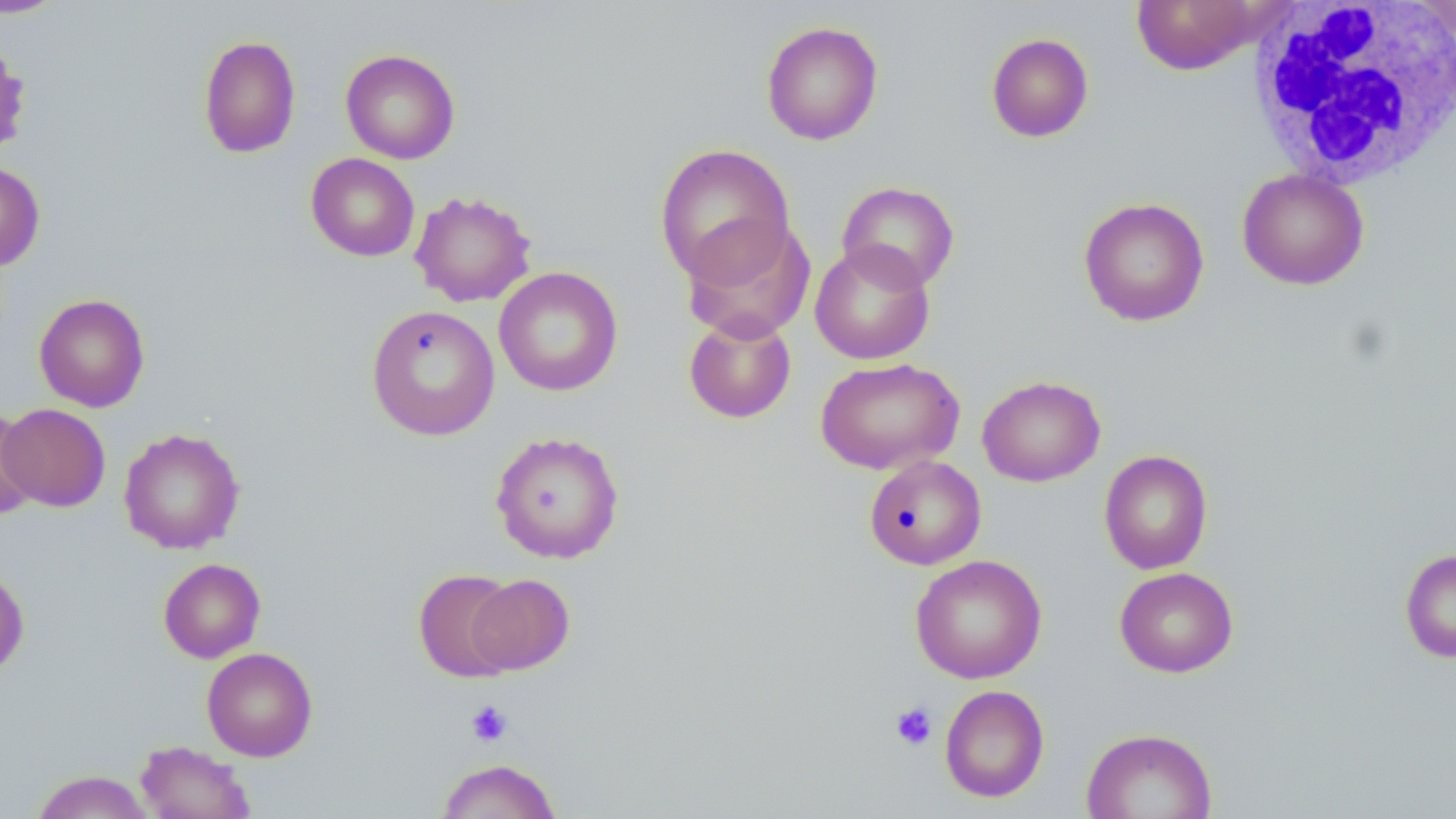

Summary:
  - Coordinate format: approximate bounding boxes as [x1, y1, x2, y2] in pixels
  - Uninfected red blood cell locations: [1128, 0, 1277, 74], [0, 1, 68, 18], [1413, 1, 1456, 43], [761, 21, 883, 145], [986, 32, 1094, 142], [197, 34, 301, 158], [340, 48, 460, 164], [654, 143, 796, 285], [305, 153, 419, 261], [0, 161, 45, 272], [1237, 168, 1369, 290], [836, 181, 960, 292], [410, 190, 536, 307], [1078, 197, 1210, 327], [680, 215, 815, 342], [810, 241, 935, 365], [493, 266, 623, 397], [34, 293, 150, 412], [366, 304, 500, 441], [683, 312, 796, 423], [815, 357, 964, 475], [977, 375, 1105, 487], [1, 404, 111, 512], [0, 408, 40, 521], [118, 427, 245, 554], [490, 431, 624, 564], [1099, 449, 1213, 573], [864, 455, 986, 570], [1399, 548, 1456, 663], [910, 554, 1047, 683], [158, 558, 266, 663], [0, 565, 30, 676], [1115, 566, 1239, 678], [413, 569, 521, 682], [466, 574, 574, 674], [202, 647, 318, 761], [939, 685, 1049, 802], [1081, 727, 1217, 819], [135, 740, 255, 819], [436, 758, 562, 818], [31, 770, 155, 818]
  - Platelet locations: [466, 701, 512, 746], [890, 701, 938, 751]
  - White blood cell locations: [1247, 0, 1456, 189]
  - Slide-level diagnosis: negative for blood parasites
  - Image size: 1456×819 pixels
  - Stain: May-Grünwald-Giemsa
  - Magnification: 1000x
  - Preparation: thin blood smear
  - Field of view: one of a larger specimen
  - Modality: optical microscopy